Give the extent of all Plasmodium parasites.
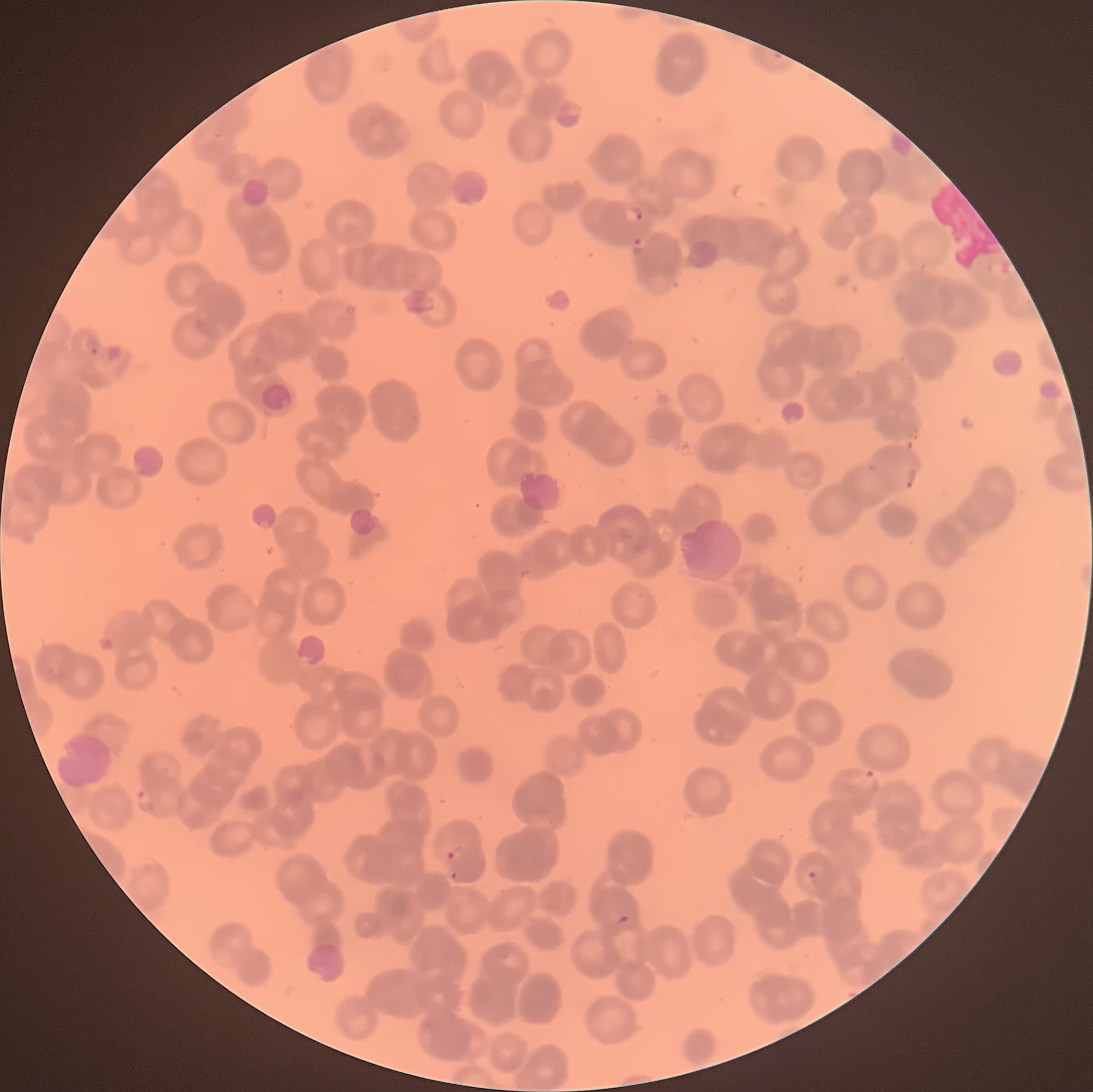
Approximate bounding boxes as (x1, y1, x2, y2) in pixels.
Plasmodium parasites: (622, 204, 645, 226), (631, 234, 645, 248), (83, 338, 102, 357), (905, 466, 917, 491), (850, 765, 878, 790), (135, 786, 159, 816), (445, 848, 457, 862), (806, 869, 817, 881), (449, 870, 460, 881), (614, 911, 631, 927).

Image is 1093×1092 pixels. The red blood cells show rouleaux formation. Light microscopy. Thin blood film.